Give the position of every Plasmodium parasite visible.
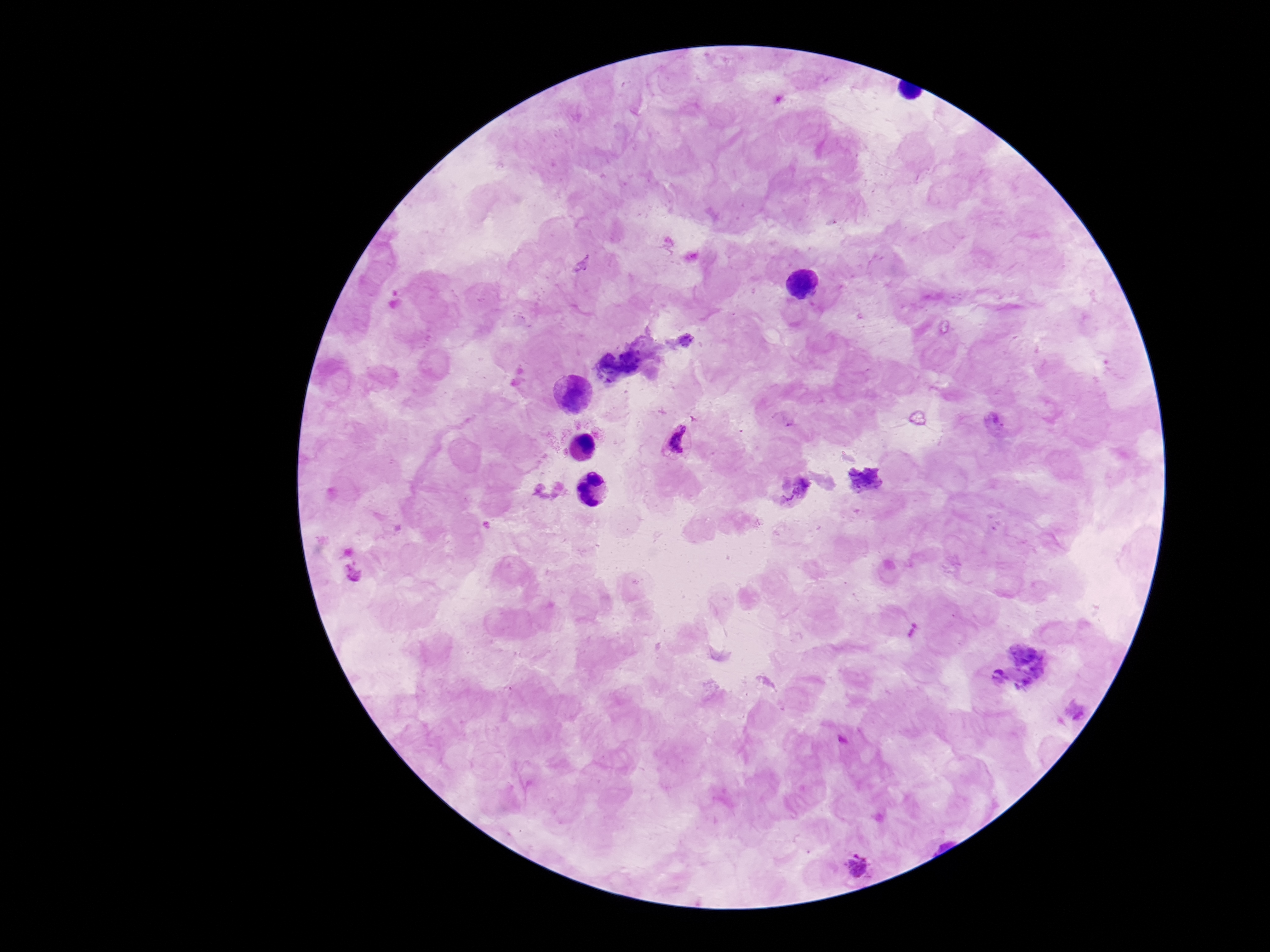

Approximate centers as (x, y) in pixels.
Plasmodium parasites: (677, 438), (354, 574), (859, 864).

100x magnification. Giemsa stain. Single field of view. Smartphone photograph taken through the microscope eyepiece. Image is 1270×952 pixels. Patient malaria status: positive. Thick blood smear.